Classify this cell by malaria status.
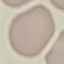
It is uninfected.

Giemsa-stained preparation. Thin blood film. Automatically extracted cell patch, resized to 64 × 64 pixels. Acquired by smartphone through the microscope eyepiece.